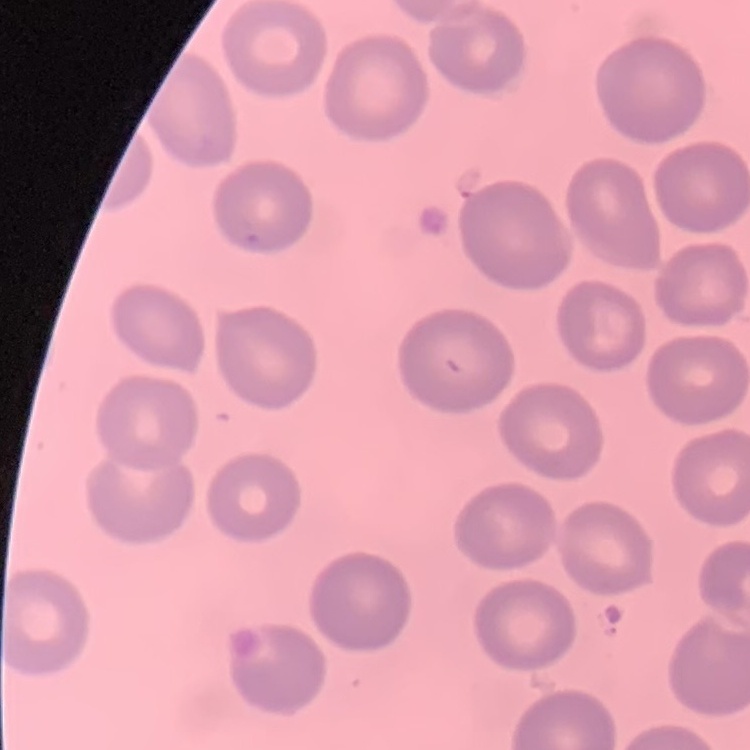

The erythrocytes exhibit no rouleaux formation. One tile cut from a larger photomicrograph. Stained with either Field's or Giemsa. Thin peripheral smear.